Describe the morphology of the red blood cells.
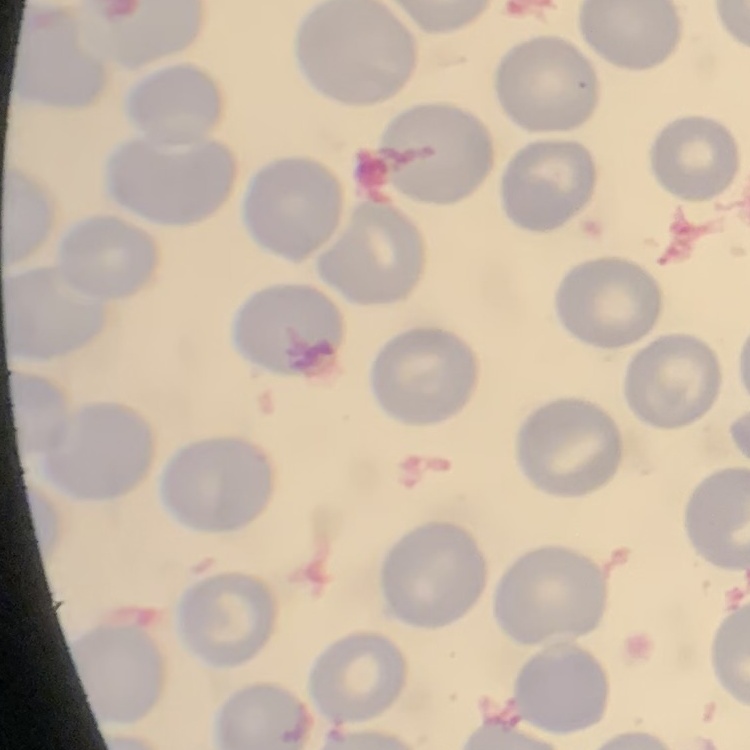
No rouleaux formation.

Summary:
  - Stain: Field's or Giemsa
  - Image type: one tile cut from a larger photomicrograph
  - Preparation: thin blood smear